State the preparation type.
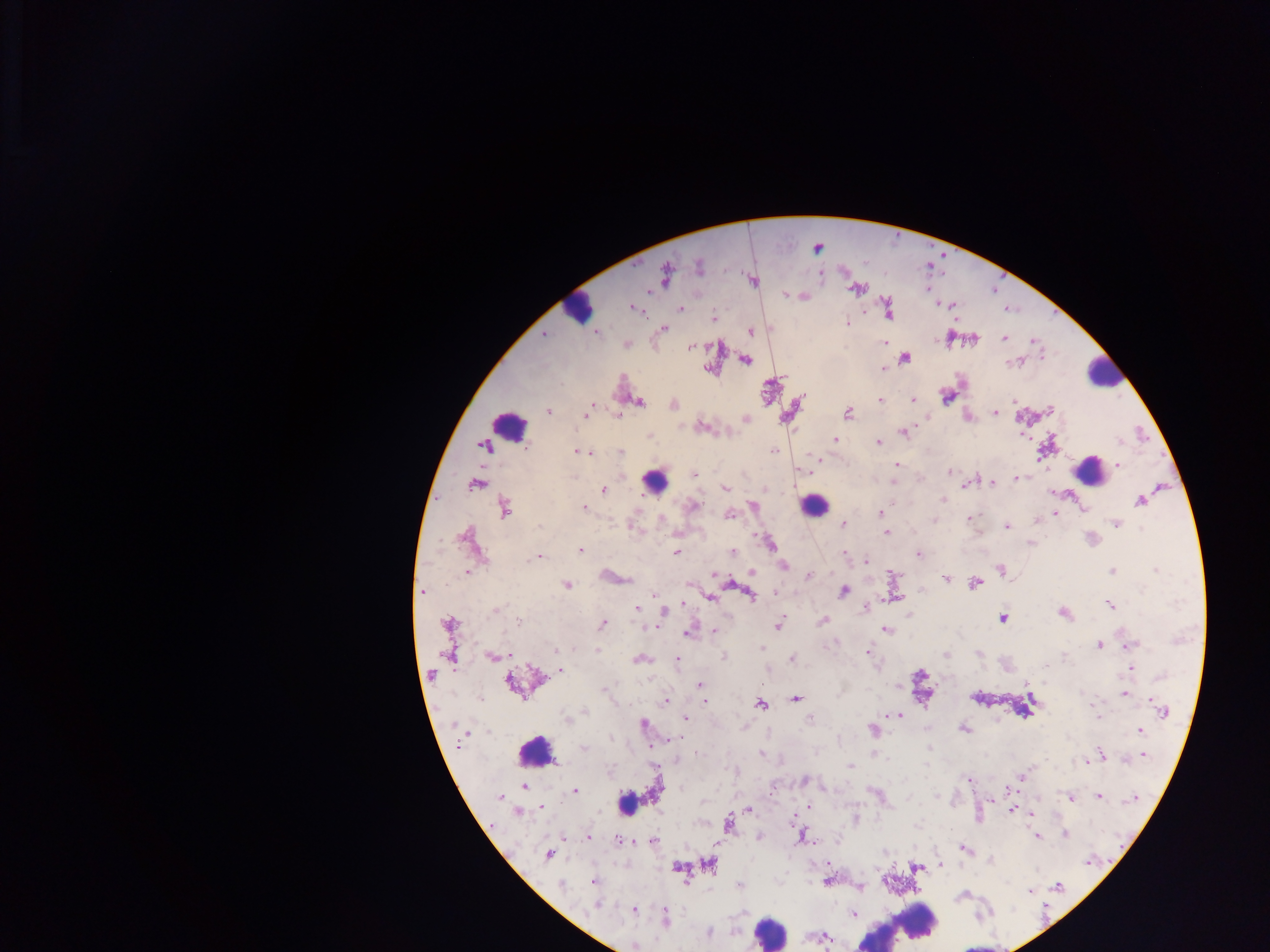
This is a thick smear.

field of view = single
malaria parasite locations = approximate centers as {x, y} in pixels: {817, 247}, {698, 266}, {665, 274}, {820, 274}, {752, 280}, {856, 288}, {785, 294}, {803, 295}, {952, 304}, {633, 307}, {888, 308}, {680, 309}, {714, 318}, {846, 323}, {662, 328}, {750, 330}, {596, 332}, {543, 333}, {1004, 338}, {949, 339}, {972, 339}, {1035, 340}, {626, 343}, {885, 343}, {690, 346}, {904, 357}, {745, 359}, {1017, 361}, {883, 368}, {709, 370}, {946, 395}, {913, 399}, {880, 401}, {638, 402}, {672, 404}, {590, 408}, {1050, 410}, {547, 411}, {847, 412}, {994, 412}, {586, 413}, {618, 415}, {966, 415}, {745, 418}, {700, 426}, {904, 431}, {649, 437}, {835, 440}, {878, 442}, {486, 445}, {1045, 448}, {774, 449}, {576, 450}, {590, 452}, {621, 452}, {583, 453}, {819, 458}, {896, 464}, {1117, 465}, {948, 472}, {694, 474}, {1015, 478}, {893, 480}, {991, 482}, {475, 484}, {965, 484}, {726, 488}, {603, 489}, {942, 500}, {1140, 500}, {752, 505}, {692, 506}, {583, 507}, {504, 508}, {1083, 510}, {880, 513}, {1055, 513}, {728, 514}, {969, 518}, {932, 520}, {1036, 520}, {842, 523}, {1116, 523}, {632, 526}, {1006, 527}, {886, 533}, {468, 539}, {1030, 542}, {769, 543}, {580, 549}, {676, 552}, {732, 552}, {843, 553}, {917, 553}, {538, 557}, {866, 561}, {782, 565}, {1000, 570}, {1112, 571}, {466, 572}, {751, 572}, {808, 576}, {893, 576}, {610, 577}, {946, 578}, {974, 583}, {688, 584}, {566, 585}, {423, 591}, {843, 591}, {774, 592}, {656, 595}, {750, 595}, {709, 596}, {891, 597}, {681, 604}, {1110, 605}, {866, 607}, {495, 609}, {636, 609}, {663, 613}, {1062, 613}, {1002, 617}, {518, 621}, {823, 621}, {448, 623}, {602, 624}, {778, 625}, {649, 626}, {885, 629}, {713, 631}, {689, 632}, {1128, 644}, {1098, 645}, {761, 646}, {868, 652}, {448, 654}, {946, 654}, {979, 654}, {492, 656}, {725, 656}, {639, 659}, {792, 659}, {677, 661}, {1131, 668}, {559, 670}, {515, 682}, {699, 685}, {899, 688}, {1123, 693}, {976, 697}, {796, 698}, {704, 700}, {664, 701}, {760, 704}, {1163, 711}, {885, 715}, {899, 715}, {684, 717}, {1097, 717}, {567, 718}, {809, 718}, {642, 724}, {871, 729}, {963, 729}, {1139, 730}, {668, 740}, {583, 749}, {930, 749}, {696, 752}, {762, 753}, {874, 755}, {1100, 755}, {1141, 755}, {851, 766}, {1021, 777}, {969, 779}, {804, 780}, {524, 787}, {574, 791}, {1098, 796}, {501, 797}, {990, 798}, {1070, 798}, {1135, 798}, {542, 805}, {809, 806}, {748, 809}, {1011, 809}, {1017, 810}, {518, 811}, {1028, 812}, {793, 818}, {854, 819}, {728, 823}, {759, 835}, {1064, 835}, {802, 836}, {1036, 836}, {587, 837}, {617, 840}, {653, 841}, {717, 843}, {965, 848}, {885, 853}, {549, 855}, {829, 863}, {710, 864}, {940, 864}, {677, 867}, {916, 867}, {593, 881}, {826, 881}, {560, 885}, {739, 885}, {1057, 886}, {860, 887}, {1029, 890}, {963, 895}, {597, 904}, {633, 909}, {852, 914}, {664, 919}, {708, 932}, {823, 937}, {634, 945}
image size = 1270×952 pixels
leukocyte locations = approximate centers as {x, y} in pixels: {578, 307}, {1104, 372}, {508, 426}, {1089, 469}, {654, 481}, {814, 504}, {535, 752}, {625, 802}, {913, 921}, {771, 930}
country = Ghana
capture = mobile-phone photograph through a microscope